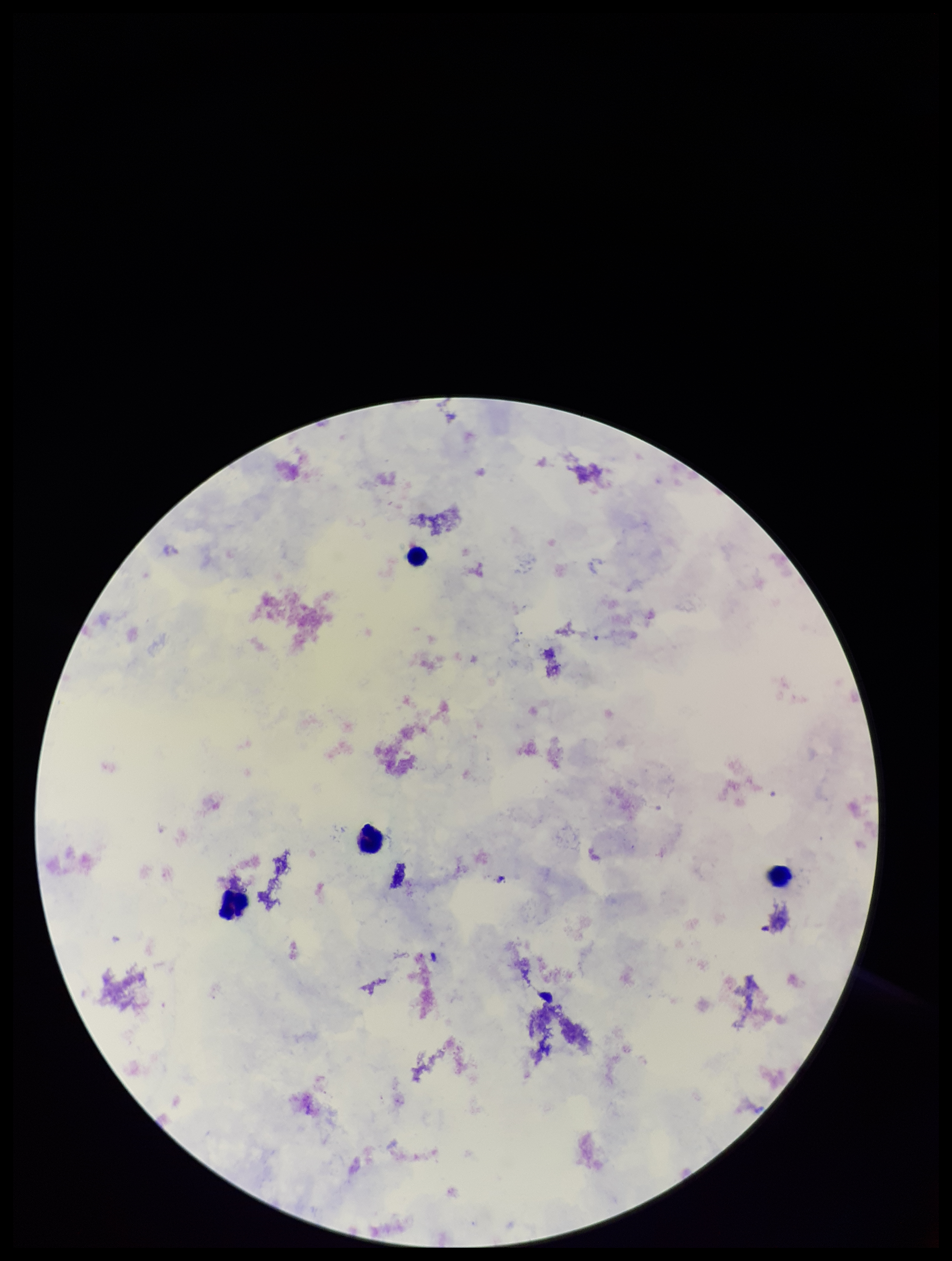
One field from this slide. Patient malaria status: negative. Preparation: thick smear. Parasite count: 0. Leukocyte count: 4. Plasmodium parasites: none seen. Stained with Giemsa. Image is 952×1261 pixels. Photographed through the microscope eyepiece with a smartphone camera.